State the preparation type.
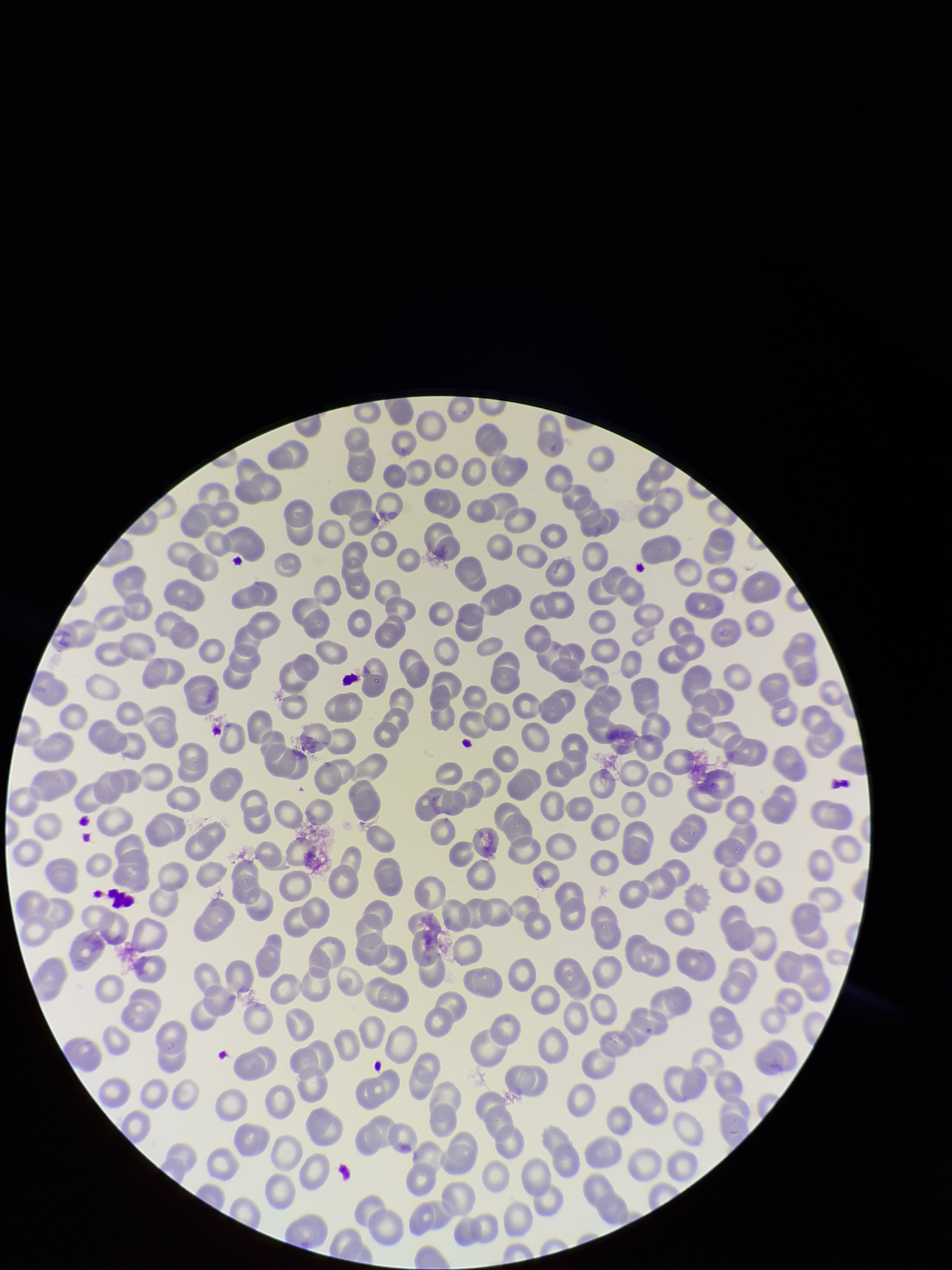

A thin smear.

red blood cell count = 288
stain = Giemsa
field of view = one from this slide
image size = 952×1270 pixels
parasitized red blood cell count = 0
patient malaria status = negative
capture = smartphone photograph through the microscope eyepiece
parasitized red blood cells = none identified